Give the extent of all Plasmodium falciparum-infected red blood cells.
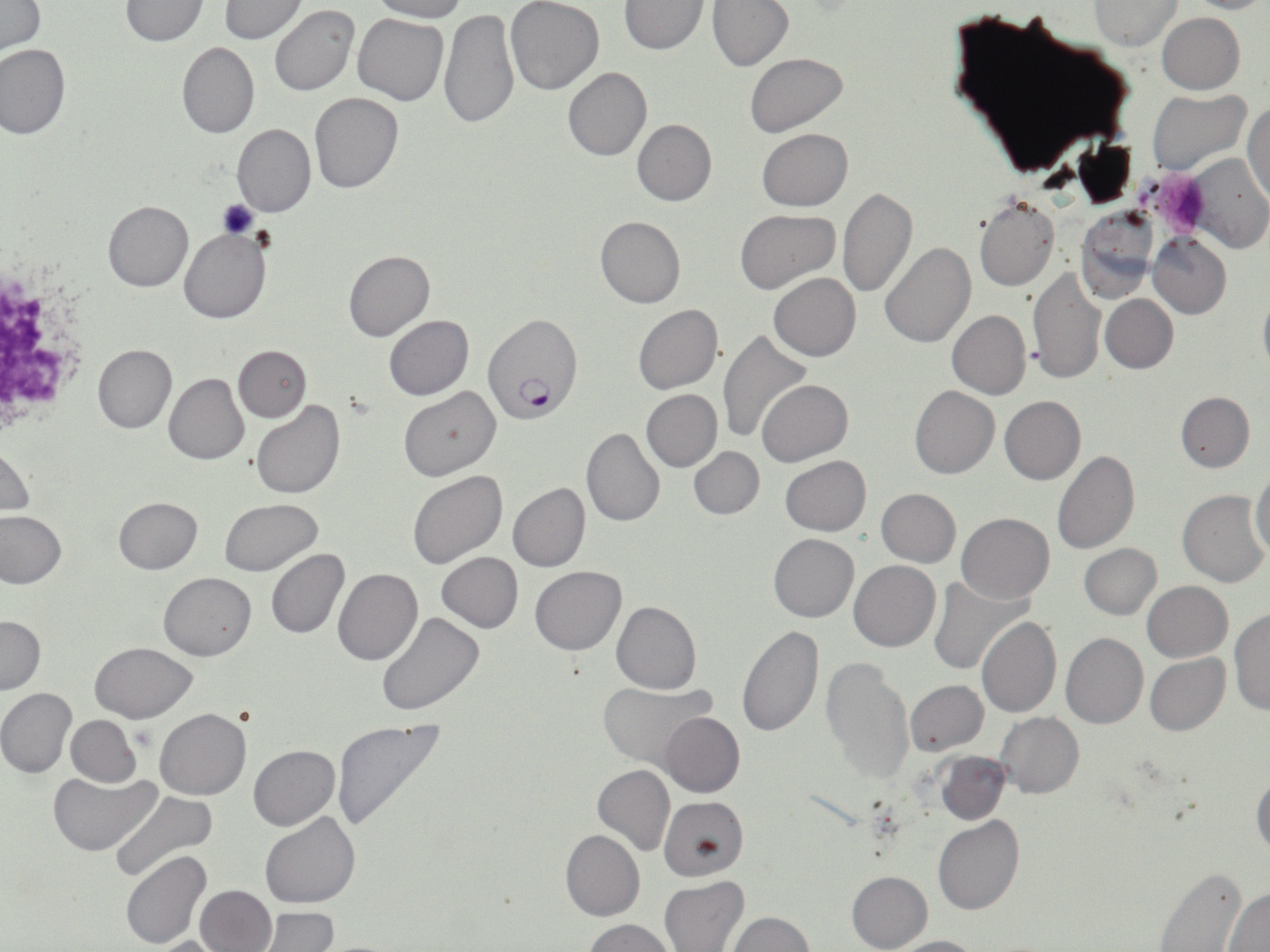

Approximate bounding boxes as (x1, y1, x2, y2) in pixels.
Plasmodium falciparum-infected red blood cells: (484, 313, 582, 426).

Platelet locations: (1151, 169, 1212, 238), (0, 283, 76, 420). Uninfected red blood cell locations: (0, 0, 46, 55), (121, 0, 207, 46), (220, 0, 305, 42), (370, 0, 466, 22), (505, 0, 604, 95), (708, 0, 793, 71), (1183, 0, 1270, 13), (618, 1, 708, 54), (1090, 1, 1180, 50), (271, 5, 358, 96), (441, 7, 519, 130), (947, 9, 1135, 178), (353, 12, 449, 105), (1157, 12, 1245, 94), (177, 41, 259, 138), (0, 43, 71, 139), (744, 54, 848, 136), (563, 67, 651, 161), (1148, 89, 1251, 175), (309, 92, 402, 194), (1245, 98, 1269, 207), (632, 118, 716, 206), (233, 123, 316, 217), (757, 128, 853, 210), (1186, 152, 1270, 254), (836, 186, 918, 298), (974, 196, 1060, 291), (102, 200, 193, 291), (736, 208, 839, 292), (1075, 211, 1158, 302), (595, 214, 685, 308), (180, 229, 270, 323), (1147, 231, 1231, 318), (1088, 240, 1166, 383), (879, 242, 975, 347), (344, 249, 434, 341), (1029, 267, 1106, 385), (768, 273, 860, 361), (1258, 289, 1270, 375), (1100, 294, 1178, 373), (632, 304, 722, 393), (947, 310, 1031, 398), (383, 315, 473, 400), (718, 328, 812, 443), (92, 343, 176, 433), (234, 346, 310, 422), (163, 372, 249, 464), (757, 378, 853, 465), (910, 385, 1000, 478), (400, 386, 500, 481), (641, 389, 722, 471), (1176, 391, 1254, 472), (1000, 395, 1085, 485), (250, 401, 345, 499), (582, 428, 664, 529), (1, 446, 35, 516), (689, 446, 765, 519), (1052, 451, 1139, 555), (781, 457, 870, 535), (406, 469, 507, 570), (1250, 469, 1270, 559), (508, 483, 590, 572), (876, 488, 960, 567), (1177, 490, 1268, 587), (114, 497, 202, 574), (218, 498, 324, 575), (0, 511, 67, 589), (957, 513, 1054, 604), (769, 533, 859, 621), (1079, 543, 1161, 618), (265, 549, 349, 639), (438, 552, 523, 632), (850, 560, 940, 652), (530, 564, 625, 654), (335, 567, 422, 665), (159, 572, 255, 660), (927, 577, 1030, 675), (1142, 581, 1232, 662), (348, 586, 447, 702), (611, 600, 701, 693), (1231, 609, 1270, 717), (375, 612, 484, 717), (0, 617, 45, 694), (976, 617, 1061, 718), (736, 625, 824, 738), (1061, 632, 1147, 729), (90, 642, 196, 722), (1145, 654, 1229, 736), (821, 655, 913, 785), (905, 680, 987, 755), (597, 683, 717, 768), (0, 688, 77, 778), (155, 708, 250, 800), (659, 711, 745, 797), (996, 712, 1083, 798), (66, 715, 141, 787), (329, 719, 447, 835), (249, 745, 339, 831), (937, 753, 1010, 824), (593, 764, 675, 856), (50, 770, 159, 855), (1251, 771, 1270, 857), (110, 790, 220, 884), (660, 796, 749, 880), (261, 812, 361, 909), (933, 815, 1025, 915), (560, 829, 644, 922), (121, 851, 211, 949), (1154, 866, 1247, 952), (847, 871, 933, 952), (659, 877, 748, 952), (195, 884, 276, 952), (1223, 888, 1270, 950), (256, 907, 337, 952), (728, 912, 813, 951), (583, 919, 677, 952), (889, 936, 981, 952), (149, 937, 231, 952). Slide-level diagnosis: Plasmodium falciparum. Thin blood film. Image is 1270×952 pixels. 1000x magnification. May-Grünwald-Giemsa-stained preparation. One field of a larger specimen. Optical microscopy.